Classify this cell by malaria status.
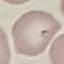
It is parasitized.

Automatically extracted cell patch, resized to 64 × 64 pixels. Acquired by smartphone through the microscope eyepiece. Giemsa stain. Thin smear of blood.